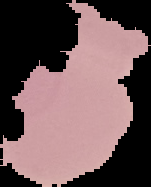

preparation = thin blood film
malaria status = uninfected
image type = cell region segmented out of the field of view; surrounding area masked to black
image size = 151×187 pixels